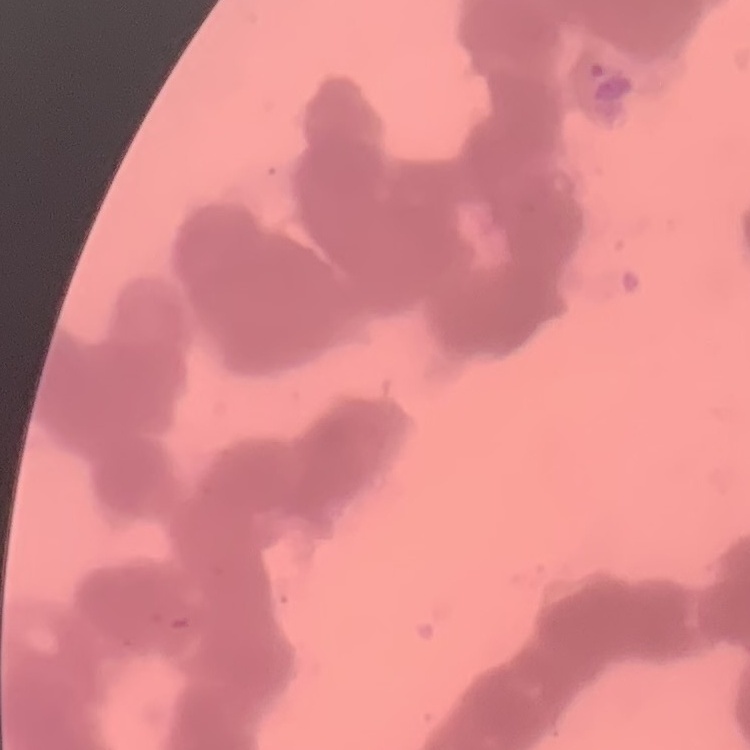 The erythrocytes exhibit rouleaux formation. Field's or Giemsa stain. One tile cut from a larger photomicrograph. Thin blood smear.